Locate every P. falciparum parasite and identify its life-cycle stage.
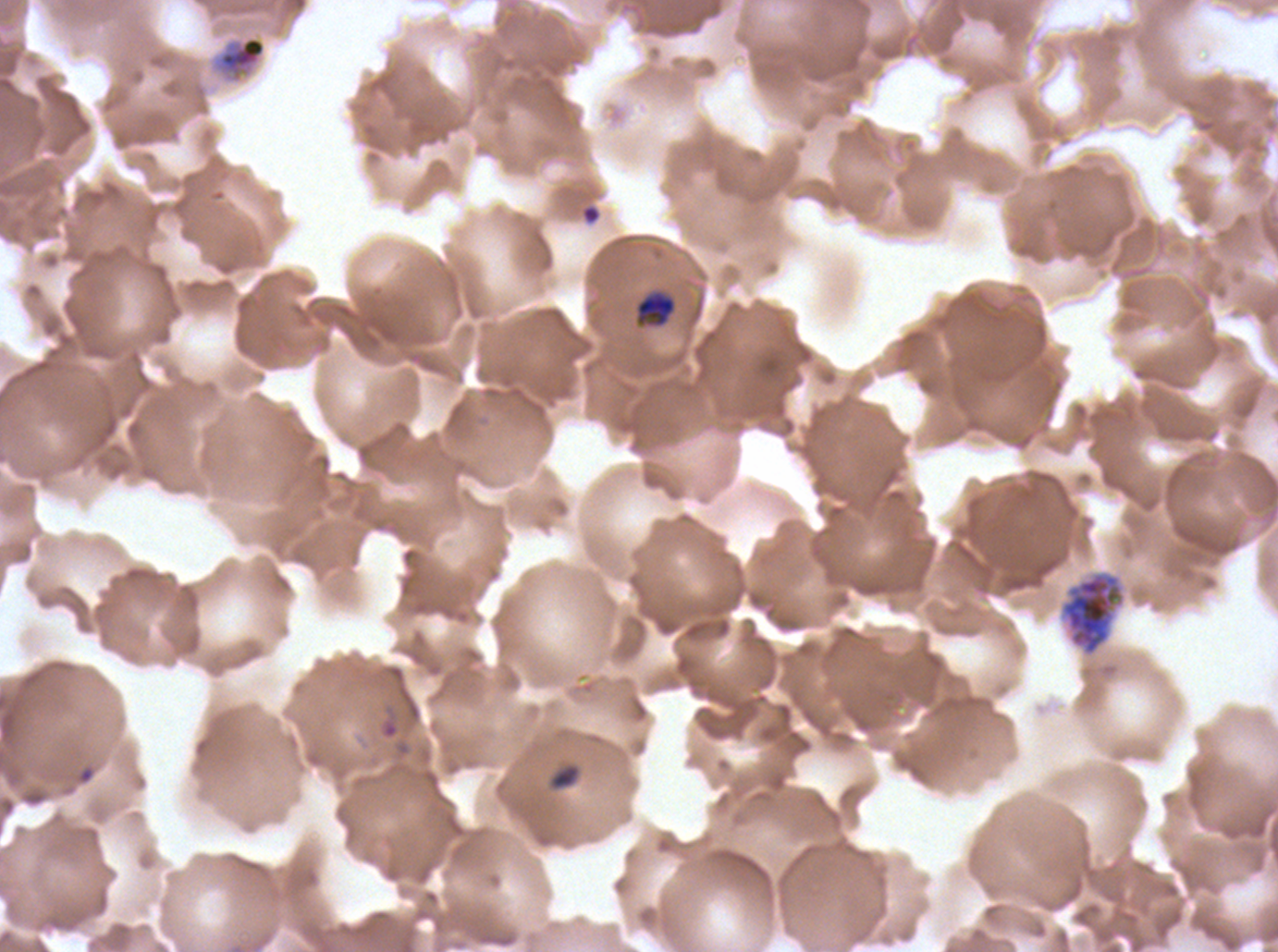

Approximate bounding boxes as [x1, y1, x2, y2] in pixels.
Late-ring/early-trophozoite forms: [547, 763, 582, 791].
Mid trophozoites: [634, 290, 677, 328].
Late trophozoites: [211, 35, 267, 84].
Early schizonts: [1059, 571, 1125, 656].
One object is labeled both ring and debris by the source: [580, 203, 602, 226].
No late schizonts, segmenters, or gametocytes observed.

Giemsa stain. Thin blood smear. One sub-image of a larger composite. Life-cycle stages observed: late-ring/early-trophozoite, mid trophozoite, late trophozoite, early schizont. P. falciparum from a patient in The Gambia, cultured ex vivo for 24 to 48 hours. Image is 1278×952 pixels.